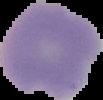
image_type: segmented cell region on a black background
malaria_status: uninfected
preparation: thin blood film
image_size: 103×100 pixels